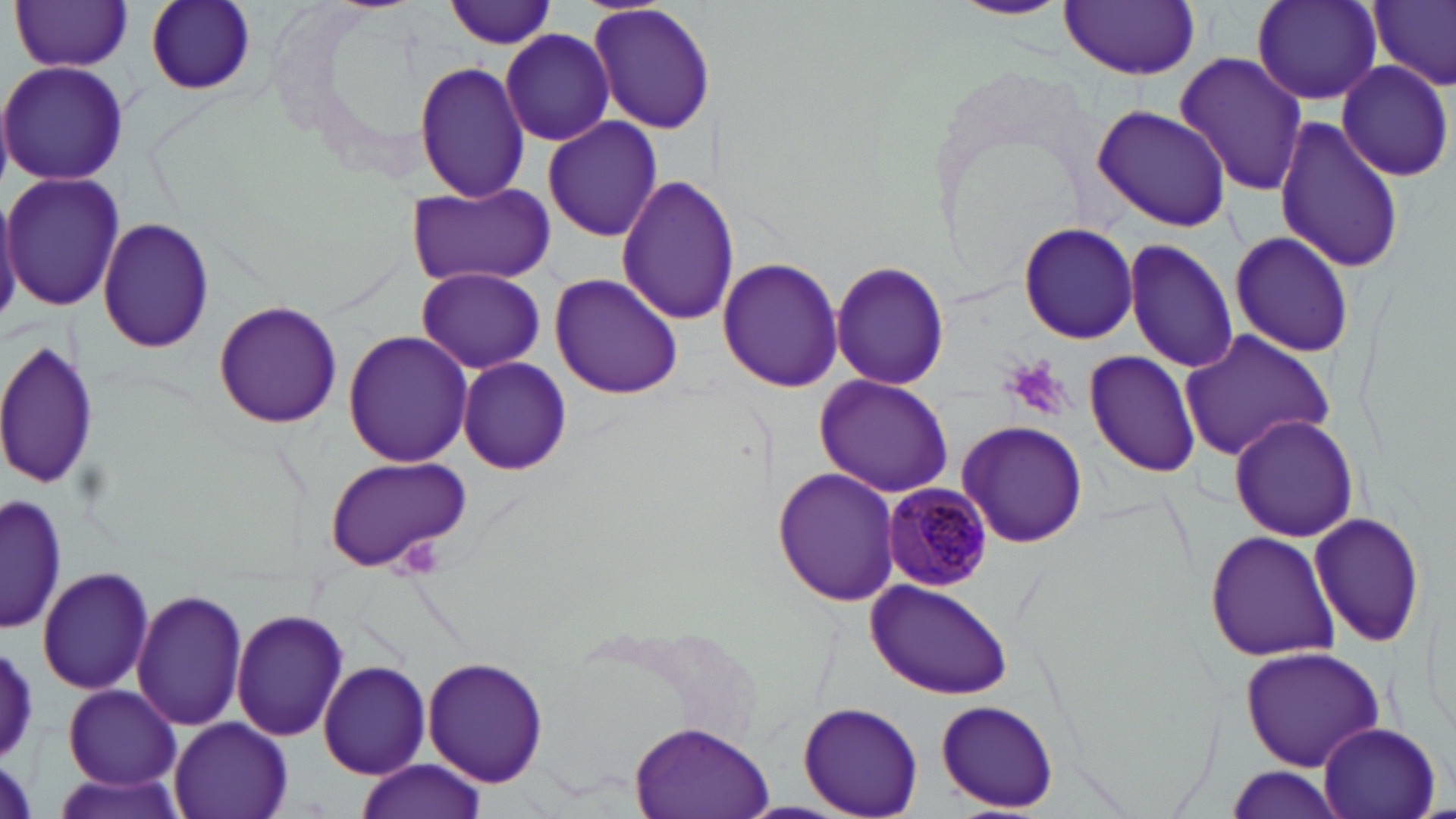

Summary:
  - Coordinate format: approximate bounding boxes as (x1,y1)-(x2,y2) corner pairs in pixels
  - Platelet locations: (1002,356)-(1074,423)
  - Plasmodium malariae-infected red blood cell locations: (883,484)-(990,590)
  - Uninfected red blood cell locations: (10,0)-(135,73), (146,0)-(257,95), (444,0)-(556,49), (948,0)-(1074,22), (1060,1)-(1200,79), (1252,1)-(1385,105), (1371,1)-(1455,91), (588,2)-(716,136), (500,29)-(617,146), (1173,52)-(1310,197), (1335,59)-(1454,183), (0,60)-(129,187), (414,60)-(531,202), (1092,103)-(1232,232), (1274,115)-(1403,276), (542,116)-(663,242), (2,170)-(123,311), (615,173)-(738,328), (406,182)-(554,288), (0,192)-(22,322), (97,218)-(215,354), (1019,222)-(1139,344), (1228,229)-(1355,358), (1123,239)-(1239,374), (717,256)-(844,394), (831,260)-(950,392), (416,267)-(546,374), (549,272)-(683,399), (213,300)-(341,428), (1178,329)-(1338,463), (342,331)-(474,469), (0,337)-(99,493), (1082,350)-(1203,479), (456,357)-(573,476), (813,373)-(953,498), (1228,414)-(1360,541), (956,420)-(1089,548), (322,456)-(473,573), (774,465)-(901,607), (1,494)-(64,637), (1309,511)-(1428,650), (1205,529)-(1340,663), (36,565)-(155,697), (864,577)-(1010,698), (132,588)-(248,729), (231,607)-(349,742), (0,639)-(41,766), (1239,647)-(1389,771), (423,657)-(549,788), (318,661)-(430,778), (62,686)-(181,789), (934,700)-(1063,812), (798,701)-(923,817), (168,717)-(292,819), (627,719)-(774,819), (1315,720)-(1440,819), (353,758)-(485,819), (1223,766)-(1346,819), (47,771)-(191,818)
  - Slide-level diagnosis: Plasmodium malariae
  - Image size: 1456×819 pixels
  - Modality: light microscopy
  - Stain: May-Grünwald-Giemsa
  - Preparation: thin blood film
  - Magnification: 1000x
  - Field of view: single